Identify the parasite.
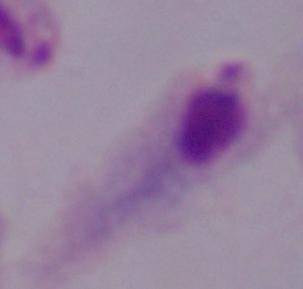
A trichomonad.

Summary:
  - Modality: micrograph
  - Magnification: 1000x